Assess this cell for malaria.
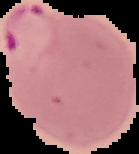
Parasitized.

preparation = thin blood smear
image size = 139×154 pixels
image type = segmented cell region on a black background